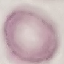 Result: negative for malaria parasites. Thin blood smear. Photographed with a smartphone camera at the microscope eyepiece. Automatically extracted cell patch, resized to 64 × 64 pixels. Giemsa stain.